Outline each Plasmodium falciparum-infected red blood cell.
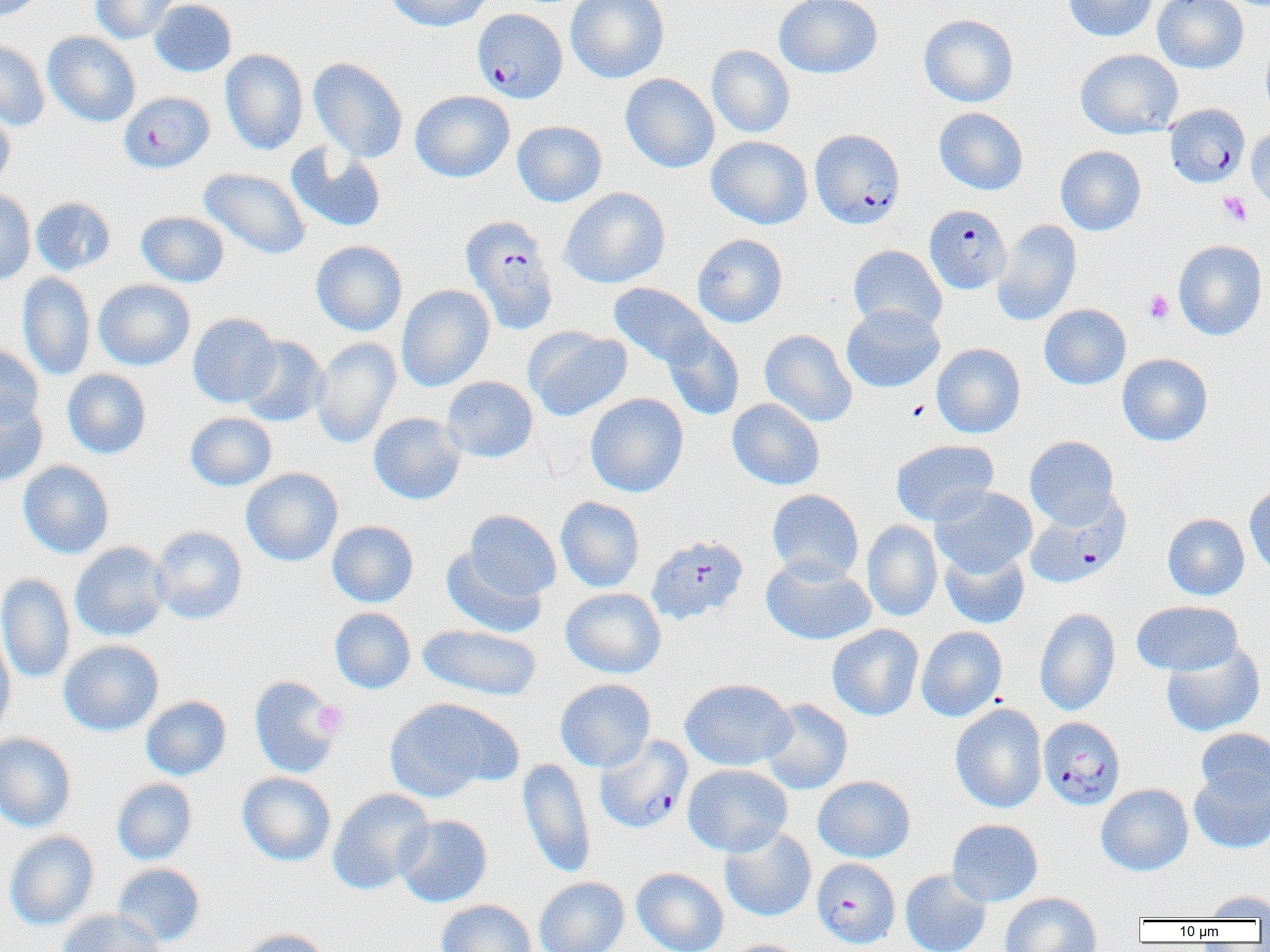

Approximate bounding boxes as named x1/y1/x2/y2 corners in pixels.
Plasmodium falciparum-infected red blood cells: (x1=472, y1=8, x2=567, y2=103), (x1=119, y1=91, x2=214, y2=173), (x1=1165, y1=103, x2=1249, y2=188), (x1=809, y1=128, x2=905, y2=229), (x1=923, y1=204, x2=1011, y2=294), (x1=460, y1=215, x2=559, y2=334), (x1=1025, y1=495, x2=1131, y2=588), (x1=645, y1=535, x2=749, y2=625), (x1=1038, y1=717, x2=1126, y2=809), (x1=594, y1=735, x2=692, y2=834), (x1=812, y1=858, x2=900, y2=949).

Summary:
  - Platelet locations: (x1=1218, y1=192, x2=1252, y2=227), (x1=1143, y1=289, x2=1174, y2=324), (x1=907, y1=400, x2=929, y2=422), (x1=312, y1=700, x2=348, y2=737)
  - Uninfected red blood cell locations: (x1=1, y1=0, x2=44, y2=24), (x1=90, y1=0, x2=181, y2=44), (x1=149, y1=0, x2=237, y2=77), (x1=385, y1=0, x2=494, y2=31), (x1=566, y1=0, x2=669, y2=83), (x1=774, y1=0, x2=883, y2=79), (x1=1063, y1=0, x2=1158, y2=42), (x1=1152, y1=0, x2=1248, y2=73), (x1=919, y1=13, x2=1018, y2=108), (x1=43, y1=32, x2=141, y2=127), (x1=0, y1=38, x2=50, y2=131), (x1=1261, y1=38, x2=1270, y2=120), (x1=706, y1=45, x2=796, y2=138), (x1=220, y1=49, x2=308, y2=155), (x1=1076, y1=49, x2=1182, y2=139), (x1=308, y1=58, x2=408, y2=162), (x1=620, y1=73, x2=720, y2=173), (x1=410, y1=90, x2=515, y2=182), (x1=0, y1=104, x2=15, y2=191), (x1=934, y1=107, x2=1028, y2=195), (x1=512, y1=120, x2=607, y2=207), (x1=1246, y1=126, x2=1270, y2=212), (x1=706, y1=135, x2=813, y2=229), (x1=286, y1=142, x2=386, y2=233), (x1=1055, y1=145, x2=1146, y2=235), (x1=199, y1=168, x2=310, y2=260), (x1=559, y1=187, x2=670, y2=288), (x1=0, y1=191, x2=36, y2=284), (x1=31, y1=197, x2=116, y2=276), (x1=136, y1=210, x2=229, y2=288), (x1=992, y1=219, x2=1082, y2=326), (x1=692, y1=233, x2=788, y2=328), (x1=1174, y1=239, x2=1267, y2=341), (x1=310, y1=240, x2=407, y2=336), (x1=848, y1=245, x2=947, y2=333), (x1=17, y1=272, x2=95, y2=381), (x1=93, y1=279, x2=196, y2=371), (x1=608, y1=282, x2=713, y2=370), (x1=396, y1=284, x2=495, y2=391), (x1=841, y1=303, x2=944, y2=393), (x1=1039, y1=304, x2=1131, y2=389), (x1=187, y1=313, x2=281, y2=407), (x1=524, y1=326, x2=631, y2=421), (x1=662, y1=327, x2=745, y2=421), (x1=760, y1=329, x2=857, y2=427), (x1=238, y1=336, x2=329, y2=426), (x1=311, y1=336, x2=401, y2=449), (x1=932, y1=343, x2=1025, y2=438), (x1=0, y1=344, x2=43, y2=429), (x1=1117, y1=353, x2=1213, y2=446), (x1=62, y1=369, x2=151, y2=459), (x1=441, y1=376, x2=538, y2=463), (x1=585, y1=393, x2=688, y2=498), (x1=0, y1=395, x2=48, y2=488), (x1=727, y1=398, x2=824, y2=490), (x1=185, y1=412, x2=277, y2=491), (x1=368, y1=412, x2=467, y2=505), (x1=1024, y1=435, x2=1120, y2=528), (x1=890, y1=439, x2=998, y2=526), (x1=18, y1=460, x2=114, y2=559), (x1=241, y1=468, x2=343, y2=566), (x1=1244, y1=485, x2=1270, y2=577), (x1=931, y1=486, x2=1037, y2=576), (x1=767, y1=488, x2=864, y2=583), (x1=556, y1=496, x2=645, y2=592), (x1=464, y1=509, x2=560, y2=600), (x1=1162, y1=513, x2=1250, y2=600), (x1=327, y1=520, x2=419, y2=607), (x1=861, y1=520, x2=943, y2=622), (x1=151, y1=525, x2=247, y2=624), (x1=70, y1=541, x2=171, y2=642), (x1=441, y1=546, x2=547, y2=638), (x1=940, y1=548, x2=1029, y2=629), (x1=761, y1=557, x2=876, y2=646), (x1=0, y1=573, x2=75, y2=685), (x1=560, y1=587, x2=666, y2=678), (x1=1132, y1=600, x2=1242, y2=676), (x1=329, y1=607, x2=416, y2=694), (x1=1034, y1=608, x2=1120, y2=716), (x1=418, y1=623, x2=541, y2=701), (x1=826, y1=624, x2=924, y2=721), (x1=916, y1=626, x2=1007, y2=721), (x1=0, y1=629, x2=15, y2=743), (x1=58, y1=639, x2=164, y2=736), (x1=1160, y1=642, x2=1265, y2=738), (x1=249, y1=675, x2=342, y2=778), (x1=555, y1=678, x2=656, y2=772), (x1=680, y1=678, x2=795, y2=770), (x1=141, y1=695, x2=231, y2=780), (x1=384, y1=698, x2=508, y2=802), (x1=761, y1=699, x2=853, y2=794), (x1=950, y1=703, x2=1047, y2=813), (x1=1195, y1=728, x2=1270, y2=807), (x1=0, y1=732, x2=77, y2=832), (x1=518, y1=758, x2=595, y2=877), (x1=683, y1=764, x2=792, y2=857), (x1=1190, y1=767, x2=1270, y2=854), (x1=237, y1=771, x2=336, y2=866), (x1=813, y1=776, x2=915, y2=863), (x1=112, y1=778, x2=198, y2=865), (x1=1096, y1=783, x2=1193, y2=876), (x1=328, y1=788, x2=435, y2=894), (x1=394, y1=814, x2=492, y2=907), (x1=947, y1=819, x2=1043, y2=906), (x1=720, y1=828, x2=816, y2=921), (x1=4, y1=831, x2=99, y2=930), (x1=112, y1=863, x2=205, y2=947), (x1=632, y1=867, x2=729, y2=952), (x1=900, y1=869, x2=991, y2=952), (x1=534, y1=876, x2=629, y2=952), (x1=1201, y1=889, x2=1270, y2=920), (x1=1000, y1=892, x2=1102, y2=952), (x1=436, y1=899, x2=535, y2=952), (x1=56, y1=908, x2=165, y2=952), (x1=238, y1=928, x2=333, y2=952), (x1=724, y1=939, x2=810, y2=952)
  - Slide-level diagnosis: Plasmodium falciparum
  - Modality: light microscopy
  - Image size: 1270×952 pixels
  - Field of view: one of a larger specimen
  - Magnification: 1000x
  - Preparation: thin blood film